Classify this cell by malaria status.
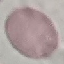
It is uninfected.

{
  "preparation": "thin blood smear",
  "image_type": "automatically extracted cell patch, resized to 64 × 64 pixels",
  "capture": "smartphone through the microscope eyepiece",
  "stain": "Giemsa"
}